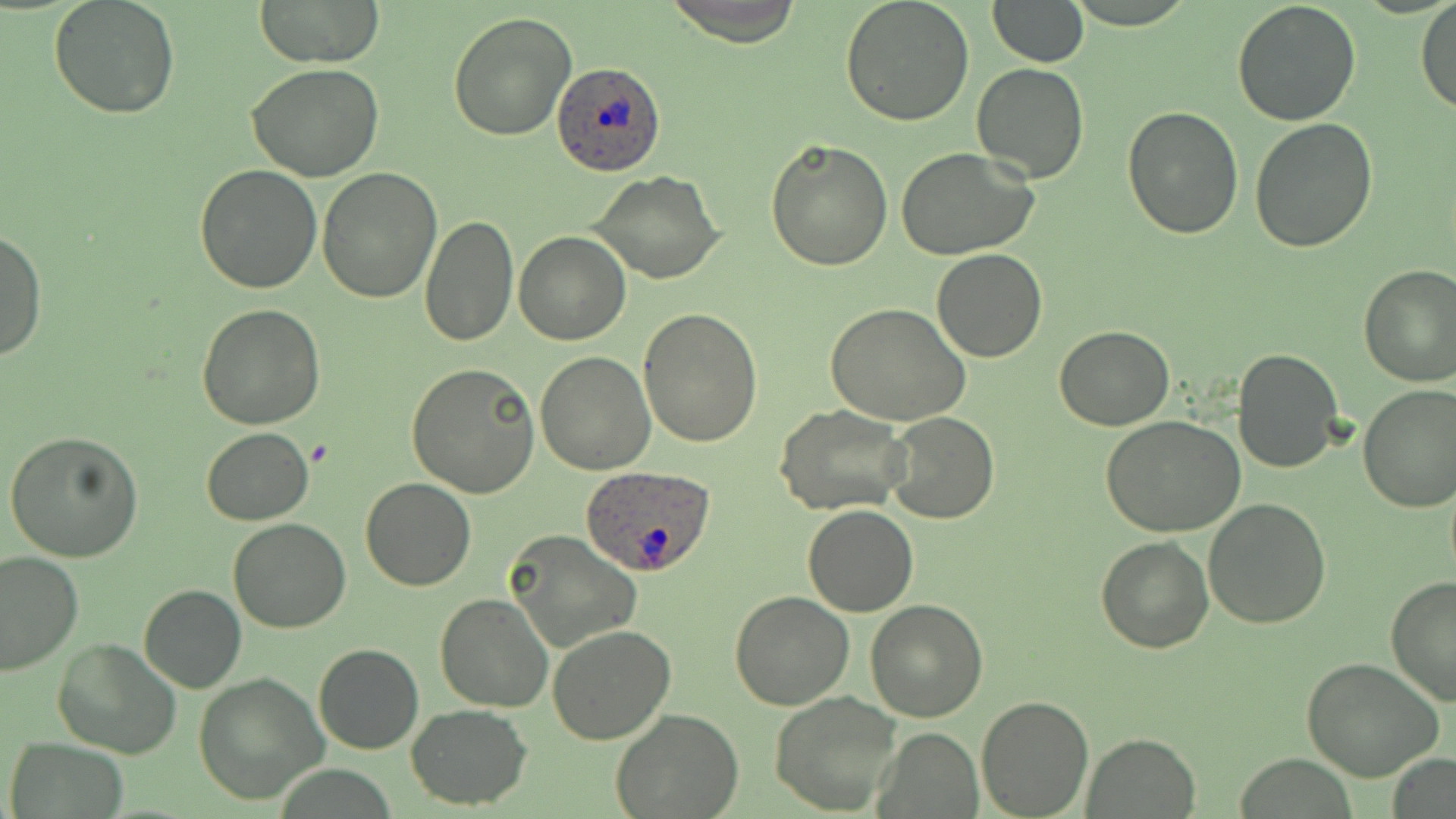
Approximate bounding boxes as named x1/y1/x2/y2 corners in pixels. Plasmodium ovale-infected red blood cell locations: (x1=552, y1=62, x2=666, y2=176), (x1=579, y1=464, x2=717, y2=576). Uninfected red blood cell locations: (x1=50, y1=0, x2=182, y2=120), (x1=253, y1=0, x2=386, y2=68), (x1=662, y1=0, x2=808, y2=46), (x1=840, y1=0, x2=974, y2=125), (x1=987, y1=0, x2=1087, y2=66), (x1=1231, y1=1, x2=1361, y2=126), (x1=1415, y1=1, x2=1456, y2=116), (x1=447, y1=10, x2=577, y2=140), (x1=971, y1=63, x2=1090, y2=183), (x1=246, y1=64, x2=386, y2=183), (x1=1121, y1=106, x2=1244, y2=240), (x1=1250, y1=118, x2=1379, y2=252), (x1=766, y1=136, x2=894, y2=270), (x1=895, y1=147, x2=1040, y2=262), (x1=194, y1=165, x2=322, y2=294), (x1=316, y1=166, x2=441, y2=303), (x1=589, y1=171, x2=725, y2=284), (x1=418, y1=214, x2=519, y2=348), (x1=1, y1=227, x2=46, y2=362), (x1=514, y1=231, x2=632, y2=345), (x1=932, y1=250, x2=1047, y2=362), (x1=1357, y1=264, x2=1456, y2=385), (x1=825, y1=302, x2=971, y2=426), (x1=197, y1=304, x2=328, y2=429), (x1=639, y1=309, x2=764, y2=448), (x1=1054, y1=326, x2=1175, y2=431), (x1=1232, y1=347, x2=1344, y2=473), (x1=534, y1=351, x2=656, y2=476), (x1=405, y1=363, x2=540, y2=498), (x1=1358, y1=385, x2=1456, y2=514), (x1=774, y1=404, x2=911, y2=515), (x1=884, y1=413, x2=1000, y2=524), (x1=1102, y1=416, x2=1249, y2=537), (x1=202, y1=427, x2=313, y2=525), (x1=5, y1=431, x2=143, y2=562), (x1=360, y1=476, x2=476, y2=592), (x1=1203, y1=498, x2=1333, y2=629), (x1=802, y1=505, x2=918, y2=617), (x1=227, y1=518, x2=351, y2=634), (x1=1096, y1=519, x2=1328, y2=642), (x1=506, y1=531, x2=642, y2=654), (x1=1096, y1=537, x2=1215, y2=655), (x1=0, y1=552, x2=84, y2=677), (x1=1385, y1=575, x2=1456, y2=706), (x1=139, y1=584, x2=245, y2=692), (x1=730, y1=592, x2=855, y2=710), (x1=434, y1=593, x2=555, y2=712), (x1=865, y1=599, x2=990, y2=721), (x1=547, y1=626, x2=676, y2=745), (x1=52, y1=635, x2=183, y2=758), (x1=313, y1=643, x2=424, y2=755), (x1=1300, y1=657, x2=1443, y2=783), (x1=194, y1=673, x2=329, y2=805), (x1=770, y1=691, x2=902, y2=815), (x1=976, y1=694, x2=1095, y2=819), (x1=406, y1=706, x2=533, y2=808), (x1=612, y1=709, x2=744, y2=818), (x1=876, y1=728, x2=983, y2=816), (x1=1083, y1=732, x2=1200, y2=817), (x1=6, y1=739, x2=130, y2=819), (x1=1389, y1=750, x2=1455, y2=819). Slide-level diagnosis: Plasmodium ovale. Thin blood smear. Single field of view. Captured at 1000x magnification. Image is 1456×819 pixels. May-Grünwald-Giemsa-stained preparation. Light microscopy.